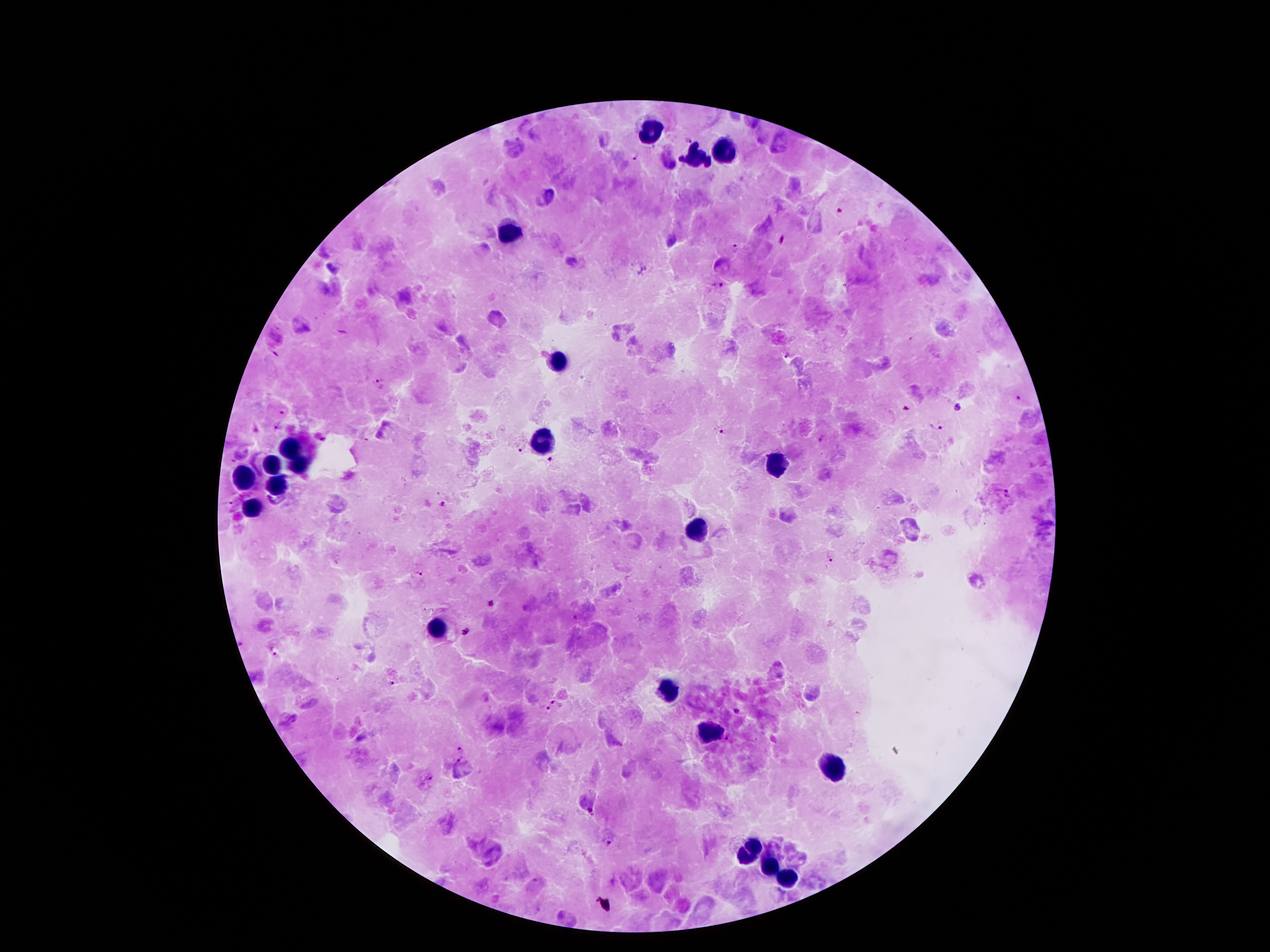

coordinate format = approximate centers as [x, y] in pixels
leukocyte locations = [648, 131], [725, 151], [693, 156], [507, 233], [557, 360], [541, 435], [287, 451], [777, 462], [271, 467], [301, 467], [241, 478], [276, 485], [251, 508], [693, 530], [437, 630], [665, 690], [707, 730], [833, 765], [756, 844], [746, 857], [774, 868], [789, 877]
Plasmodium parasite locations = [685, 138], [635, 156], [840, 212], [782, 240], [734, 248], [717, 285], [787, 353], [379, 385], [1018, 399], [957, 406], [905, 408], [283, 411], [277, 427], [719, 429], [936, 430], [822, 437], [521, 450], [547, 458], [1008, 493], [230, 502], [442, 504], [831, 557], [419, 574], [491, 602], [466, 632], [273, 650], [392, 684], [555, 701], [545, 708], [737, 710], [463, 751], [458, 761], [430, 776], [592, 810], [608, 840]
patient malaria status = infected with Plasmodium falciparum
preparation = thick blood film
magnification = 100x
capture = smartphone through the microscope eyepiece
field of view = one from this slide
stain = Giemsa
image size = 1270×952 pixels